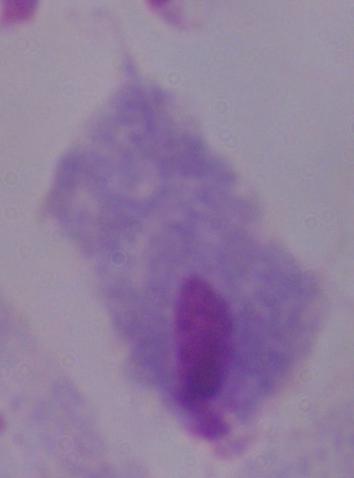

identification = trichomonad
magnification = 1000x
modality = photomicrograph